State which cell type is depicted.
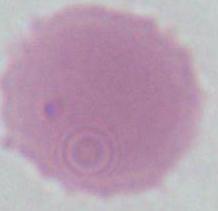
An erythrocyte.

1000x magnification. Photomicrograph.